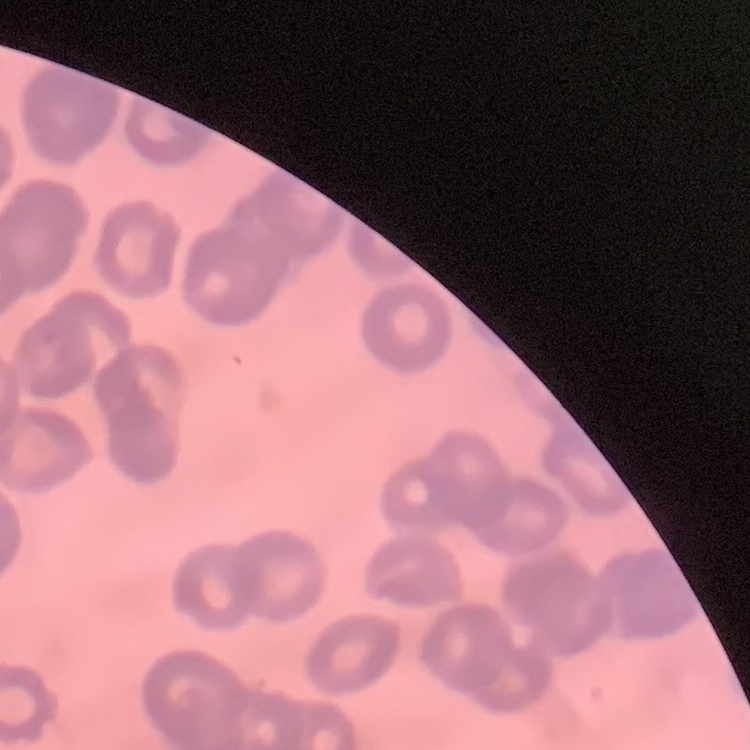

Summary:
  - Red blood cell morphology: rouleaux formation
  - Preparation: thin blood smear
  - Image type: square crop of a larger photomicrograph
  - Stain: Field's or Giemsa